Identify the preparation type.
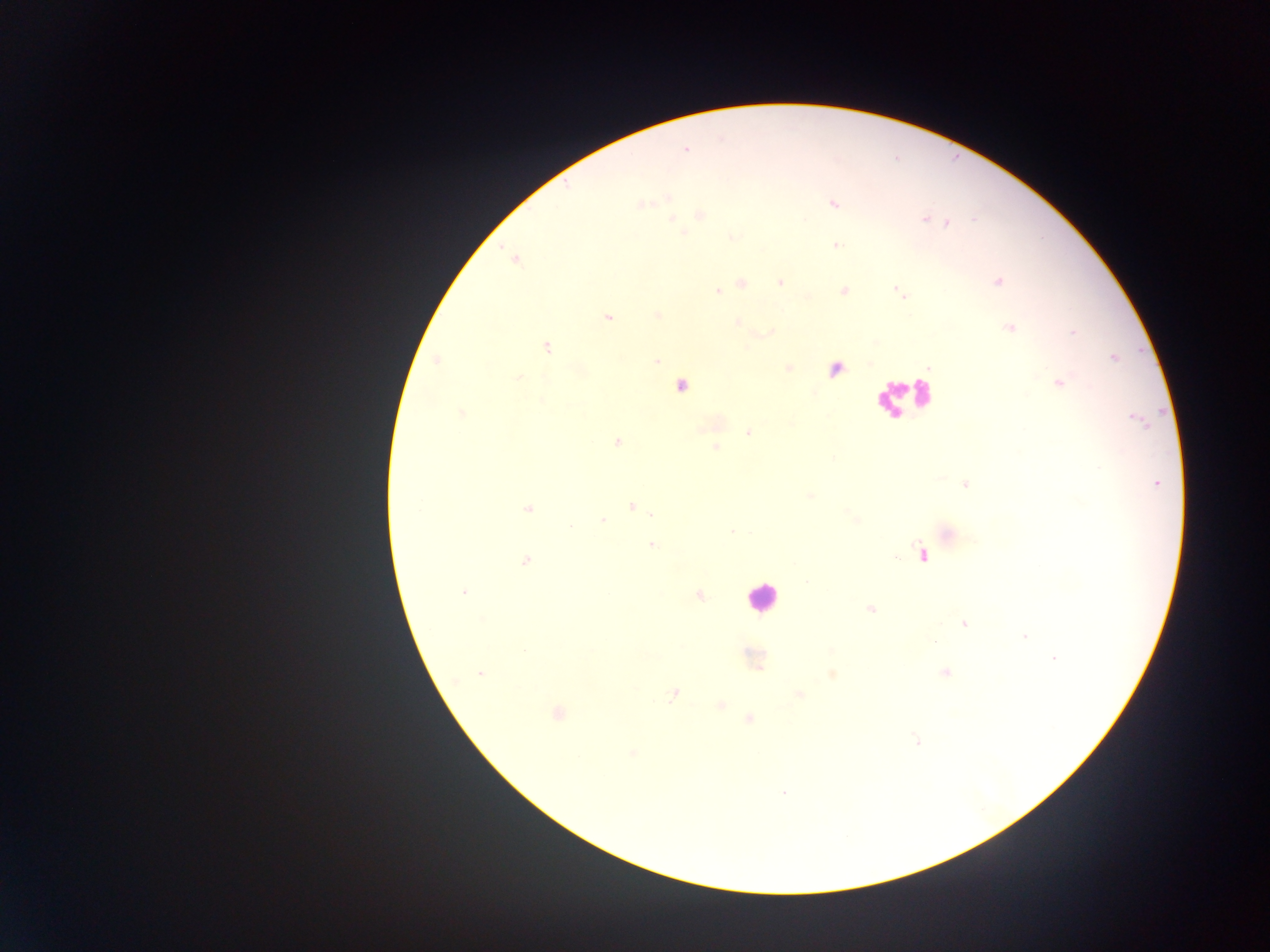

This is a thick smear.

Approximate centers as (x, y) in pixels. Plasmodium parasite locations: (684, 149), (834, 203), (641, 204), (700, 215), (671, 218), (923, 218), (947, 223), (837, 246), (514, 258), (997, 280), (780, 281), (742, 283), (718, 291), (844, 291), (898, 292), (657, 314), (607, 317), (735, 323), (1010, 328), (545, 347), (655, 359), (437, 360), (788, 368), (837, 369), (517, 377), (1058, 382), (680, 385), (462, 414), (749, 432), (616, 441), (715, 448), (1155, 483), (965, 484), (631, 505), (528, 509), (602, 519), (652, 545), (921, 555), (526, 560), (464, 592), (698, 595), (870, 608), (965, 623), (1025, 636), (934, 642), (753, 658), (1054, 658), (946, 672), (479, 673), (831, 674), (673, 693), (797, 694), (720, 705), (557, 713), (749, 718), (917, 740), (632, 754), (783, 792). Leukocyte locations: (905, 397), (762, 597). Photographed through a microscope with a mobile-phone camera. Image is 1270×952 pixels. Sample from Ghana. One field of view.